Assess this cell for malaria.
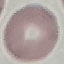
Uninfected.

Summary:
  - Stain: Giemsa
  - Capture: smartphone through the microscope eyepiece
  - Preparation: thin blood smear
  - Image type: cell patch, automatically extracted from a larger field of view and resized to 64 × 64 pixels